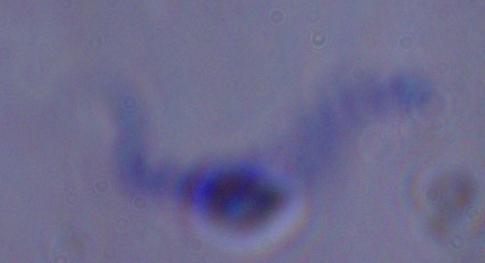
{
  "magnification": "1000x",
  "identification": "trypanosome",
  "modality": "photomicrograph"
}